Assess for Plasmodium parasites.
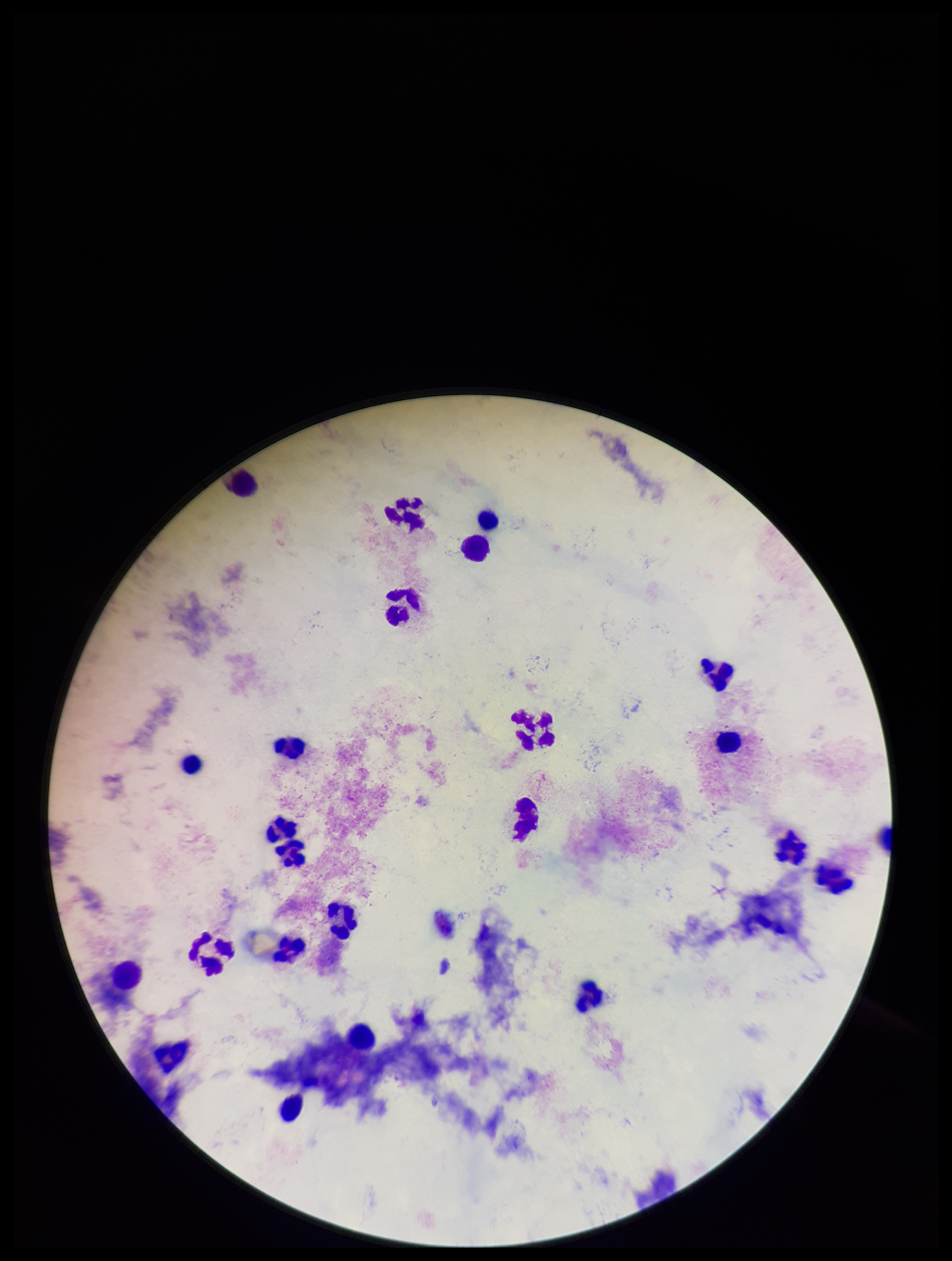
None seen.

stain = Giemsa
preparation = thick smear
image size = 952×1261 pixels
capture = smartphone photograph through the microscope eyepiece
leukocyte count = 24
field of view = one from this slide
patient malaria status = negative
parasite count = 0